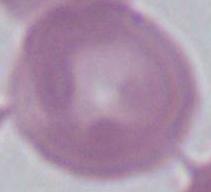 1000x magnification. A red blood cell is shown. Micrograph.